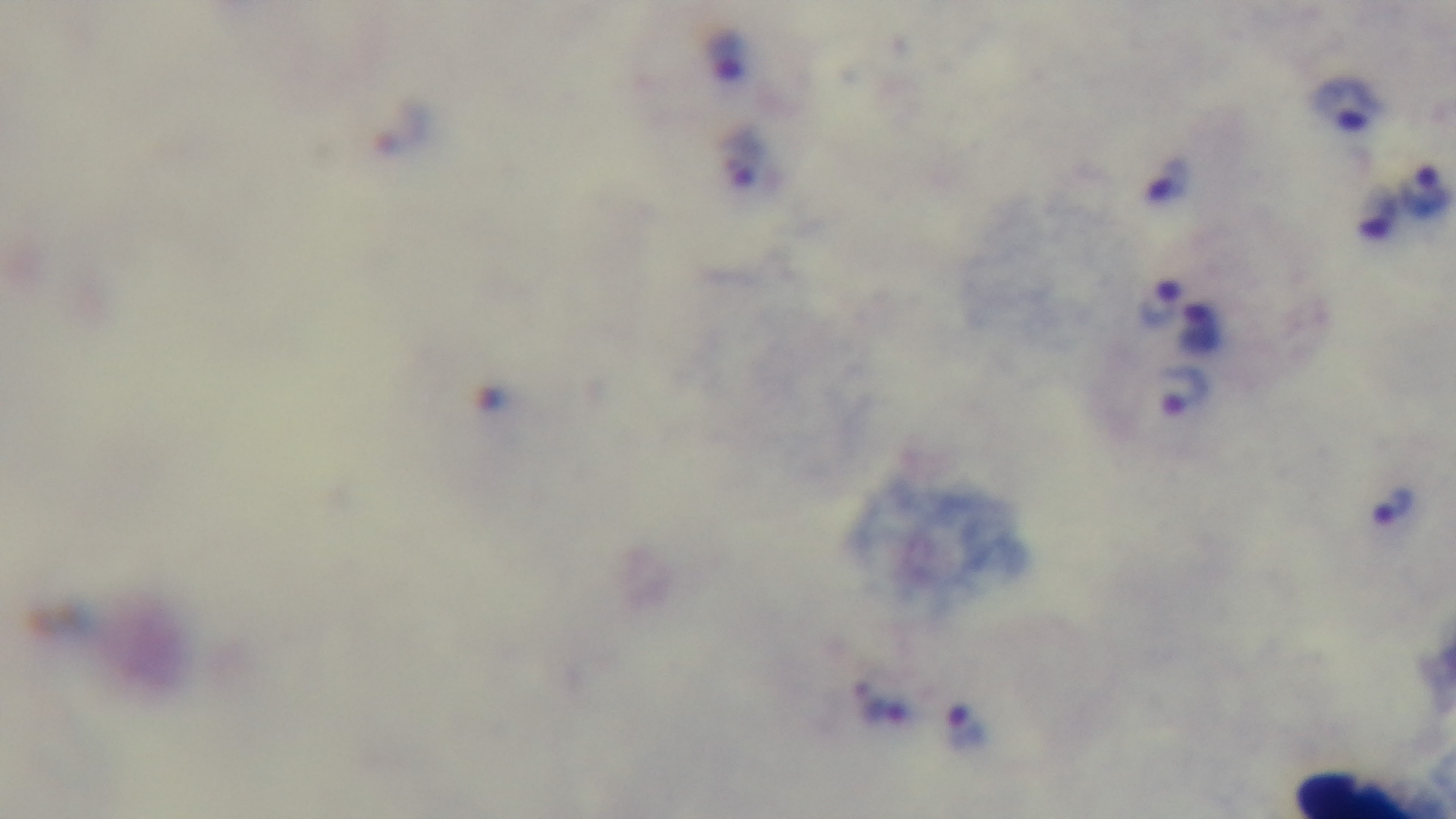
field of view = one from the slide
objective = 100x oil immersion
capture = mounted 4K digital camera
preparation = thick
modality = light microscopy
stain = Giemsa
malaria status = positive